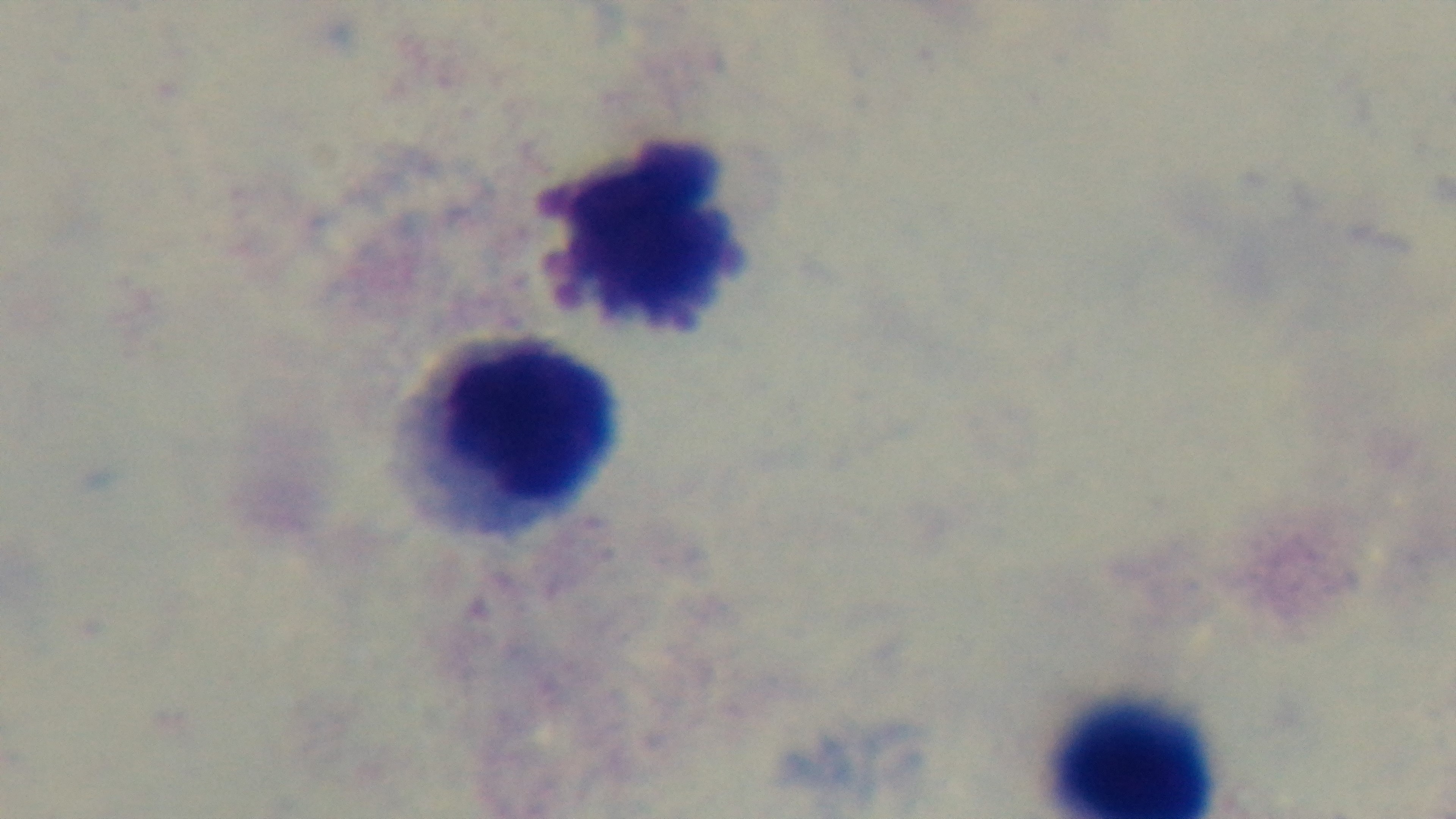 Mounted 4K digital camera. Malaria status: uninfected. Oil-immersion objective, 100x. Photomicrograph. Single field of view. Giemsa-stained. Preparation: thick smear.